Locate and identify every blood parasite.
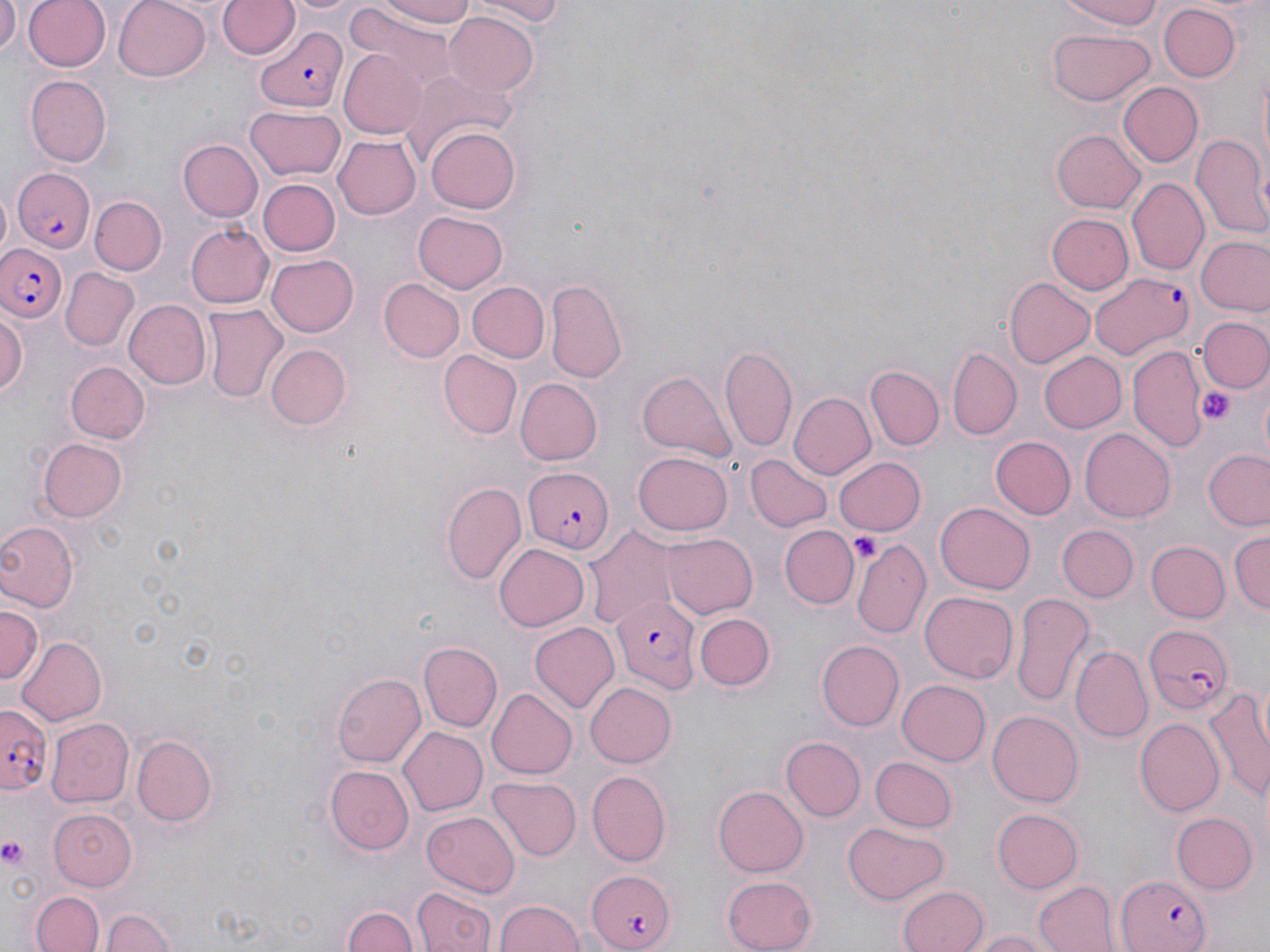

Approximate bounding boxes as (x1, y1, x2, y2) in pixels.
Plasmodium falciparum-infected red blood cells: (255, 26, 348, 111), (10, 169, 97, 252), (0, 242, 67, 326), (1089, 271, 1192, 359), (521, 465, 610, 554), (612, 596, 701, 693), (1141, 621, 1232, 712), (0, 702, 52, 791), (587, 867, 678, 952), (1115, 874, 1210, 952).
No Plasmodium ovale, Plasmodium malariae, Plasmodium vivax, Babesia divergens, or Trypanosoma brucei observed.

Platelet locations: (1200, 386, 1234, 427), (853, 533, 880, 559), (0, 835, 28, 870). Uninfected red blood cell locations: (0, 0, 22, 60), (24, 0, 111, 72), (113, 0, 214, 82), (218, 0, 299, 60), (290, 0, 358, 18), (375, 0, 479, 26), (463, 0, 574, 24), (1050, 0, 1169, 28), (1157, 4, 1242, 83), (342, 7, 460, 91), (443, 12, 539, 98), (1048, 29, 1154, 105), (338, 46, 431, 138), (399, 73, 512, 173), (25, 74, 112, 167), (1119, 83, 1204, 168), (244, 107, 347, 183), (427, 127, 519, 212), (1052, 129, 1146, 214), (1191, 133, 1270, 242), (335, 135, 421, 219), (177, 138, 262, 222), (256, 177, 339, 257), (1126, 178, 1209, 277), (91, 194, 166, 275), (412, 211, 510, 293), (1044, 213, 1133, 296), (183, 222, 274, 309), (1196, 236, 1269, 317), (265, 254, 358, 336), (60, 269, 140, 352), (546, 277, 629, 383), (1004, 277, 1095, 368), (378, 279, 464, 363), (468, 281, 549, 362), (122, 299, 210, 390), (202, 304, 287, 402), (0, 307, 26, 402), (1195, 316, 1268, 392), (266, 343, 353, 430), (719, 343, 797, 450), (1127, 343, 1209, 452), (949, 345, 1021, 439), (439, 350, 523, 438), (1038, 351, 1128, 434), (64, 360, 149, 445), (866, 366, 945, 450), (637, 370, 738, 460), (518, 377, 602, 464), (787, 391, 877, 480), (1080, 428, 1176, 522), (992, 436, 1077, 518), (38, 437, 131, 522), (1203, 449, 1270, 530), (633, 452, 733, 536), (746, 453, 833, 533), (835, 456, 926, 535), (441, 482, 526, 587), (935, 501, 1034, 595), (0, 521, 76, 613), (779, 524, 858, 610), (1059, 525, 1137, 601), (586, 526, 675, 629), (1229, 526, 1270, 617), (659, 533, 757, 618), (852, 538, 929, 639), (1144, 541, 1229, 622), (495, 543, 589, 631), (920, 591, 1018, 683), (1011, 592, 1096, 707), (1, 606, 42, 687), (695, 613, 775, 691), (530, 621, 620, 711), (17, 638, 108, 725), (818, 640, 904, 731), (420, 642, 502, 731), (1072, 646, 1154, 741), (332, 672, 426, 769), (898, 680, 992, 766), (584, 681, 676, 768), (485, 688, 577, 779), (1203, 688, 1270, 800), (986, 709, 1084, 806), (44, 717, 132, 809), (1136, 718, 1222, 814), (396, 726, 487, 816), (130, 732, 220, 827), (781, 736, 865, 820), (870, 757, 956, 833), (326, 764, 415, 855), (585, 771, 670, 868), (486, 777, 579, 861), (714, 783, 811, 875), (47, 807, 138, 891), (992, 807, 1084, 892), (421, 811, 519, 898), (1170, 812, 1257, 894), (844, 821, 947, 904), (722, 873, 817, 951), (1033, 879, 1117, 952), (897, 884, 990, 952), (411, 888, 495, 952), (33, 891, 105, 952), (495, 896, 583, 952), (343, 904, 416, 952), (99, 908, 181, 952), (964, 929, 1055, 952). Slide-level diagnosis: Plasmodium falciparum. Image is 1270×952 pixels. Thin blood smear. Captured at 1000x magnification. Optical microscopy. May-Grünwald-Giemsa-stained preparation. Single field of view.